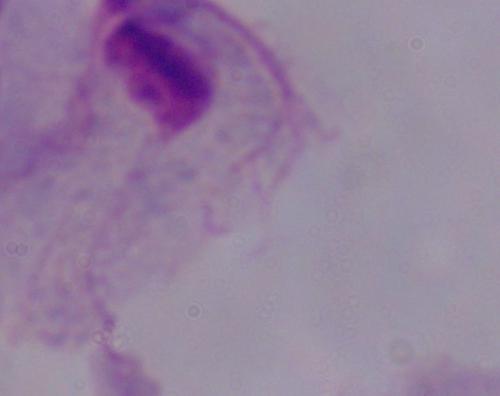 A trichomonad is seen. 1000x magnification. Photomicrograph.